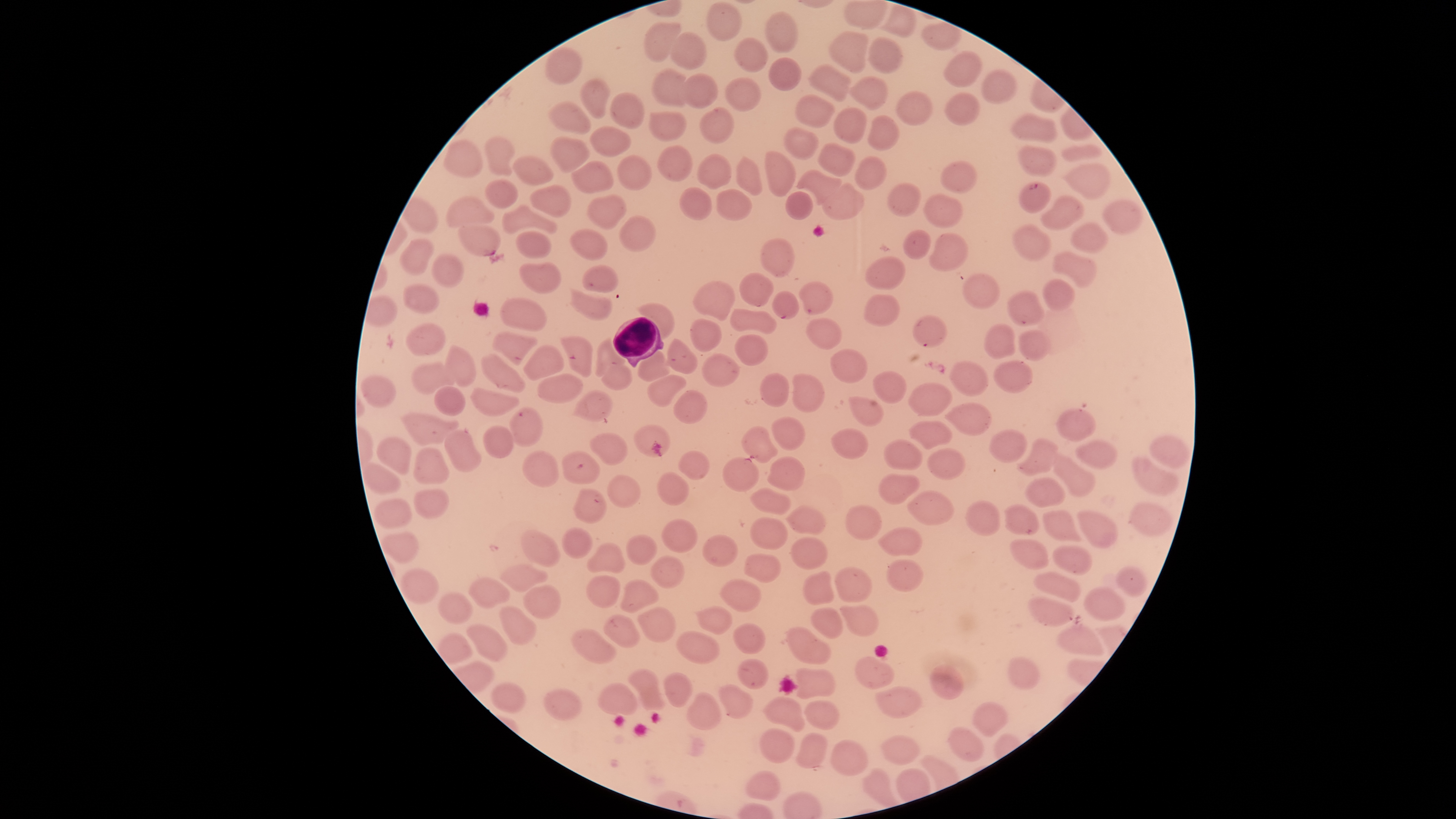

stain = Giemsa
field of view = single
parasitized red blood cells = approximate bounding boxes as {left, top, right, bottom} in pixels: {460, 226, 500, 255}, {742, 425, 778, 462}, {722, 457, 759, 492}
visible region = circular
capture = smartphone photograph through the microscope eyepiece
species = Plasmodium falciparum
presence = malaria parasites detected
white blood cells = approximate bounding boxes as {left, top, right, bottom} in pixels: {612, 317, 664, 367}
image size = 1456×819 pixels
preparation = thin blood smear
uninfected red blood cells = approximate bounding boxes as {left, top, right, bottom} in pixels: {707, 1, 742, 41}, {884, 6, 916, 36}, {766, 12, 797, 52}, {644, 21, 679, 63}, {922, 23, 960, 50}, {830, 31, 868, 72}, {670, 32, 707, 69}, {869, 37, 904, 76}, {735, 38, 767, 72}, {546, 48, 581, 82}, {944, 54, 979, 87}, {766, 56, 803, 92}, {809, 65, 850, 101}, {654, 71, 687, 107}, {980, 71, 1016, 103}, {681, 72, 720, 110}, {851, 76, 888, 108}, {581, 77, 611, 118}, {727, 77, 761, 111}, {895, 92, 934, 127}, {611, 93, 644, 129}, {946, 93, 981, 126}, {795, 94, 835, 127}, {549, 102, 592, 136}, {833, 105, 870, 142}, {700, 106, 735, 143}, {648, 112, 687, 142}, {868, 116, 899, 151}, {1012, 116, 1059, 143}, {590, 126, 631, 158}, {784, 127, 818, 158}, {486, 136, 515, 177}, {552, 136, 588, 172}, {441, 140, 483, 176}, {820, 143, 855, 176}, {657, 146, 694, 181}, {1020, 146, 1056, 175}, {1062, 146, 1102, 161}, {766, 151, 794, 198}, {617, 155, 651, 191}, {697, 155, 732, 188}, {735, 156, 764, 196}, {514, 157, 552, 185}, {855, 157, 886, 187}, {571, 161, 613, 194}, {940, 163, 975, 193}, {1064, 163, 1110, 200}, {797, 171, 842, 204}, {486, 179, 517, 208}, {822, 184, 864, 220}, {885, 184, 922, 216}, {531, 187, 569, 217}, {679, 187, 711, 221}, {717, 190, 751, 221}, {786, 191, 813, 219}, {589, 194, 626, 229}, {924, 195, 961, 228}, {1042, 196, 1085, 229}, {445, 197, 494, 227}, {1105, 202, 1141, 234}, {501, 205, 558, 234}, {621, 217, 658, 250}, {1073, 224, 1105, 253}, {1016, 227, 1050, 259}, {570, 230, 607, 262}, {519, 231, 551, 259}, {902, 231, 931, 260}, {930, 233, 967, 269}, {398, 237, 434, 274}, {760, 237, 796, 276}, {1053, 252, 1096, 287}, {431, 255, 464, 287}, {865, 256, 905, 288}, {519, 262, 564, 294}, {582, 265, 618, 294}, {739, 273, 773, 306}, {963, 275, 1000, 308}, {1044, 279, 1074, 311}, {692, 282, 734, 322}, {797, 282, 832, 315}, {404, 284, 437, 314}, {571, 290, 612, 320}, {772, 291, 800, 320}, {1008, 292, 1045, 326}, {862, 295, 899, 326}, {501, 299, 548, 331}, {639, 304, 674, 339}, {730, 309, 776, 334}, {912, 316, 947, 350}, {690, 319, 723, 352}, {806, 319, 842, 349}, {407, 324, 446, 354}, {984, 324, 1014, 359}, {1019, 330, 1051, 361}, {493, 332, 538, 364}, {736, 334, 769, 366}, {561, 336, 593, 376}, {596, 340, 626, 377}, {667, 340, 697, 375}, {522, 344, 564, 379}, {444, 345, 476, 387}, {637, 348, 669, 381}, {831, 349, 867, 383}, {481, 355, 526, 394}, {703, 355, 739, 386}, {993, 359, 1033, 394}, {414, 360, 456, 396}, {950, 360, 987, 396}, {602, 365, 632, 391}, {872, 369, 907, 404}, {361, 374, 396, 409}, {760, 374, 789, 407}, {793, 374, 824, 414}, {536, 375, 582, 404}, {647, 376, 685, 409}, {907, 383, 951, 416}, {435, 387, 463, 416}, {471, 387, 519, 418}, {673, 390, 707, 426}, {574, 391, 611, 420}, {850, 396, 883, 427}, {947, 404, 989, 436}, {1056, 406, 1097, 442}, {509, 407, 543, 445}, {403, 413, 459, 445}, {771, 418, 807, 452}, {908, 422, 952, 450}, {634, 425, 670, 459}, {484, 427, 515, 457}, {445, 429, 480, 471}, {831, 429, 868, 458}, {992, 430, 1025, 462}, {589, 433, 627, 466}, {377, 436, 412, 475}, {1150, 437, 1190, 465}, {886, 440, 922, 471}, {1017, 440, 1059, 475}, {1077, 441, 1117, 470}, {414, 446, 448, 484}, {927, 449, 966, 482}, {563, 451, 600, 484}, {679, 451, 710, 481}, {522, 452, 559, 486}, {1053, 456, 1094, 496}, {766, 457, 806, 491}, {1135, 458, 1176, 498}, {364, 462, 400, 494}, {657, 470, 688, 505}, {878, 474, 920, 505}, {608, 475, 640, 508}, {1026, 479, 1065, 507}, {574, 488, 606, 524}, {751, 488, 790, 514}, {413, 489, 450, 519}, {907, 490, 954, 524}, {375, 499, 412, 528}, {966, 501, 1000, 536}, {1004, 504, 1038, 535}, {1130, 504, 1173, 537}, {845, 505, 881, 539}, {786, 507, 826, 535}, {1044, 510, 1080, 542}, {1077, 511, 1117, 548}, {751, 518, 787, 550}, {660, 519, 697, 553}, {879, 527, 924, 557}, {562, 528, 594, 559}, {383, 531, 420, 563}, {522, 532, 560, 567}, {626, 533, 659, 566}, {704, 535, 738, 567}, {791, 536, 828, 571}, {1011, 539, 1047, 568}, {588, 543, 627, 574}, {1055, 544, 1092, 573}, {745, 554, 778, 583}, {651, 556, 684, 589}, {887, 560, 923, 592}, {501, 563, 547, 593}, {1118, 567, 1148, 596}, {834, 568, 873, 604}, {401, 571, 438, 603}, {801, 572, 834, 607}, {1035, 572, 1080, 602}, {588, 576, 620, 607}, {469, 578, 510, 609}, {721, 578, 760, 613}, {620, 580, 658, 613}, {523, 586, 560, 618}, {1084, 589, 1125, 620}, {438, 593, 471, 624}, {1029, 598, 1074, 625}, {841, 604, 878, 635}, {501, 605, 535, 645}, {698, 606, 732, 634}, {638, 607, 676, 642}, {812, 609, 843, 639}, {604, 613, 640, 648}, {468, 623, 506, 661}, {733, 623, 766, 655}, {789, 625, 830, 664}, {572, 628, 617, 665}, {1059, 628, 1105, 661}, {678, 631, 719, 663}, {856, 656, 894, 687}, {737, 657, 768, 689}, {1008, 657, 1041, 689}, {930, 665, 963, 699}, {796, 668, 835, 699}, {628, 670, 664, 710}, {665, 674, 692, 707}, {489, 682, 525, 711}, {601, 683, 637, 715}, {720, 685, 752, 719}, {875, 687, 921, 718}, {544, 689, 581, 720}, {686, 694, 722, 730}, {764, 698, 804, 730}, {805, 701, 840, 730}, {974, 701, 1007, 736}, {949, 728, 983, 762}, {761, 730, 795, 763}, {796, 733, 826, 767}, {882, 736, 919, 765}, {831, 741, 868, 775}, {747, 773, 780, 801}